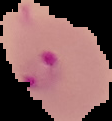 Image is 112×121 pixels. The area outside the segmented cell region is set to black. From a thin blood smear. Malaria status: parasitized.